Assess this cell for malaria.
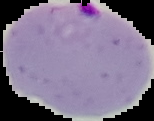
Parasitized.

{
  "image_size": "154×121 pixels",
  "preparation": "thin blood smear",
  "image_type": "segmented cell region with the area outside set to black"
}